Locate every leukocyte (white blood cell).
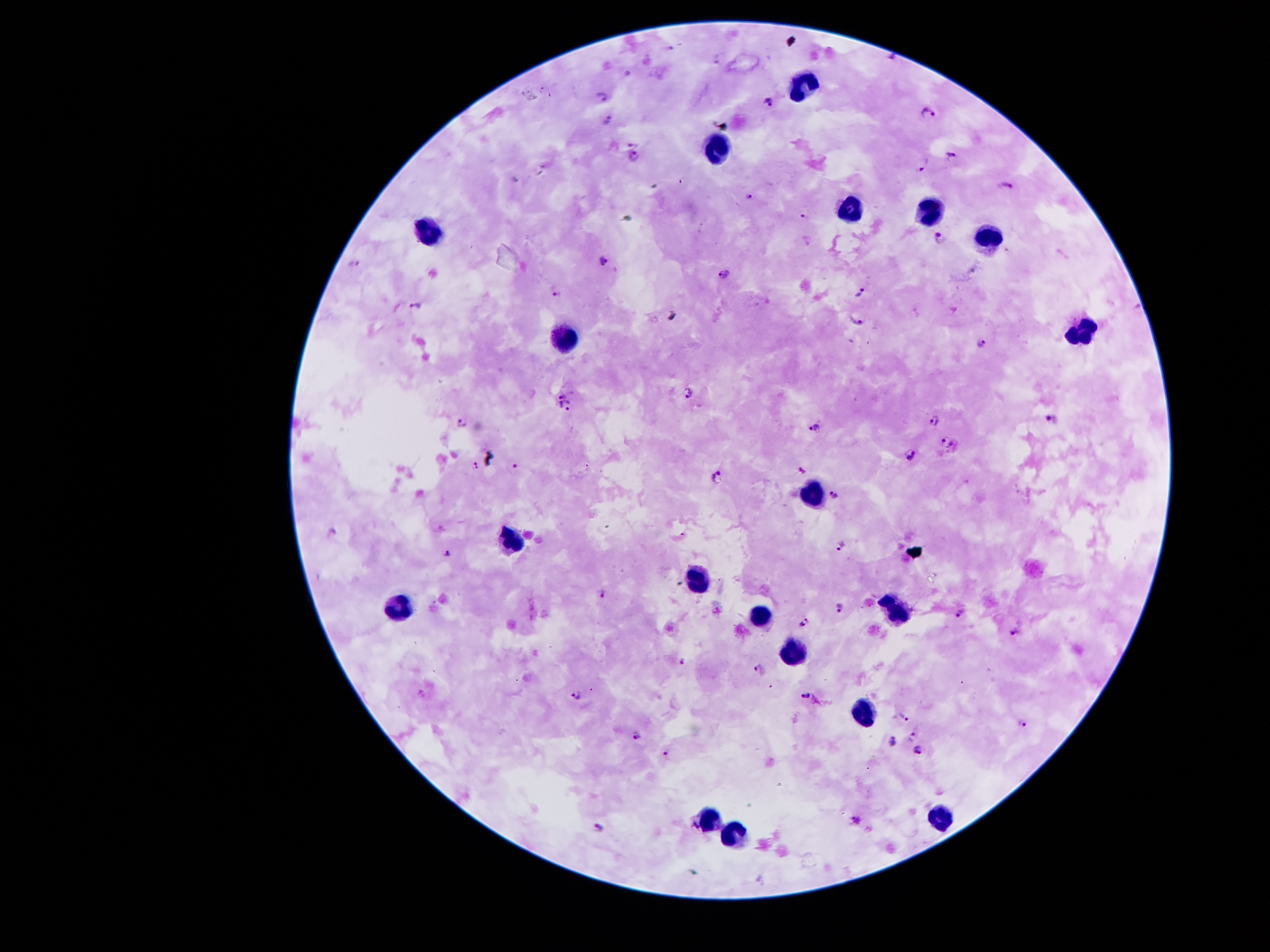

Approximate centers as (x, y) in pixels.
Leukocytes: (805, 82), (716, 148), (849, 211), (931, 212), (427, 228), (988, 236), (1079, 333), (566, 342), (815, 493), (511, 544), (693, 580), (398, 609), (893, 611), (758, 616), (791, 652), (864, 714), (940, 816), (710, 819), (733, 834).

Summary:
  - Malaria parasite locations: (718, 58), (602, 96), (767, 100), (926, 113), (608, 120), (633, 141), (634, 156), (951, 157), (923, 165), (1006, 185), (750, 197), (938, 239), (354, 262), (602, 262), (723, 274), (860, 290), (555, 292), (414, 305), (857, 321), (981, 342), (687, 393), (563, 394), (566, 409), (1050, 417), (934, 420), (461, 423), (814, 427), (946, 442), (910, 455), (475, 465), (513, 467), (717, 477), (834, 496), (842, 543), (447, 553), (602, 592), (839, 607), (960, 613), (803, 621), (1015, 630), (683, 659), (761, 668), (804, 693), (574, 695), (904, 718), (1025, 723), (636, 732), (911, 737), (892, 742), (916, 752), (664, 753), (859, 820), (599, 827)
  - Field of view: one from this slide
  - Capture: smartphone through the microscope eyepiece
  - Image size: 1270×952 pixels
  - Patient malaria status: positive for Plasmodium falciparum
  - Stain: Giemsa
  - Magnification: 100x
  - Preparation: thick blood film